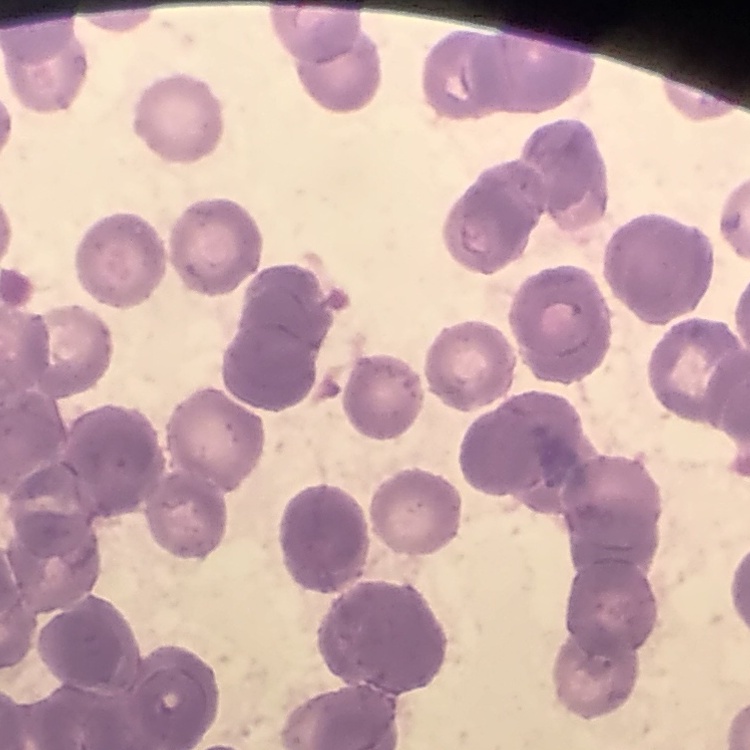

erythrocyte morphology = rouleaux formation
image type = square crop of a larger photomicrograph
stain = Field's or Giemsa
preparation = thin blood smear